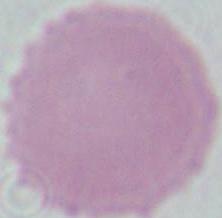

identification = erythrocyte
magnification = 1000x
modality = photomicrograph